Name the blood parasite species.
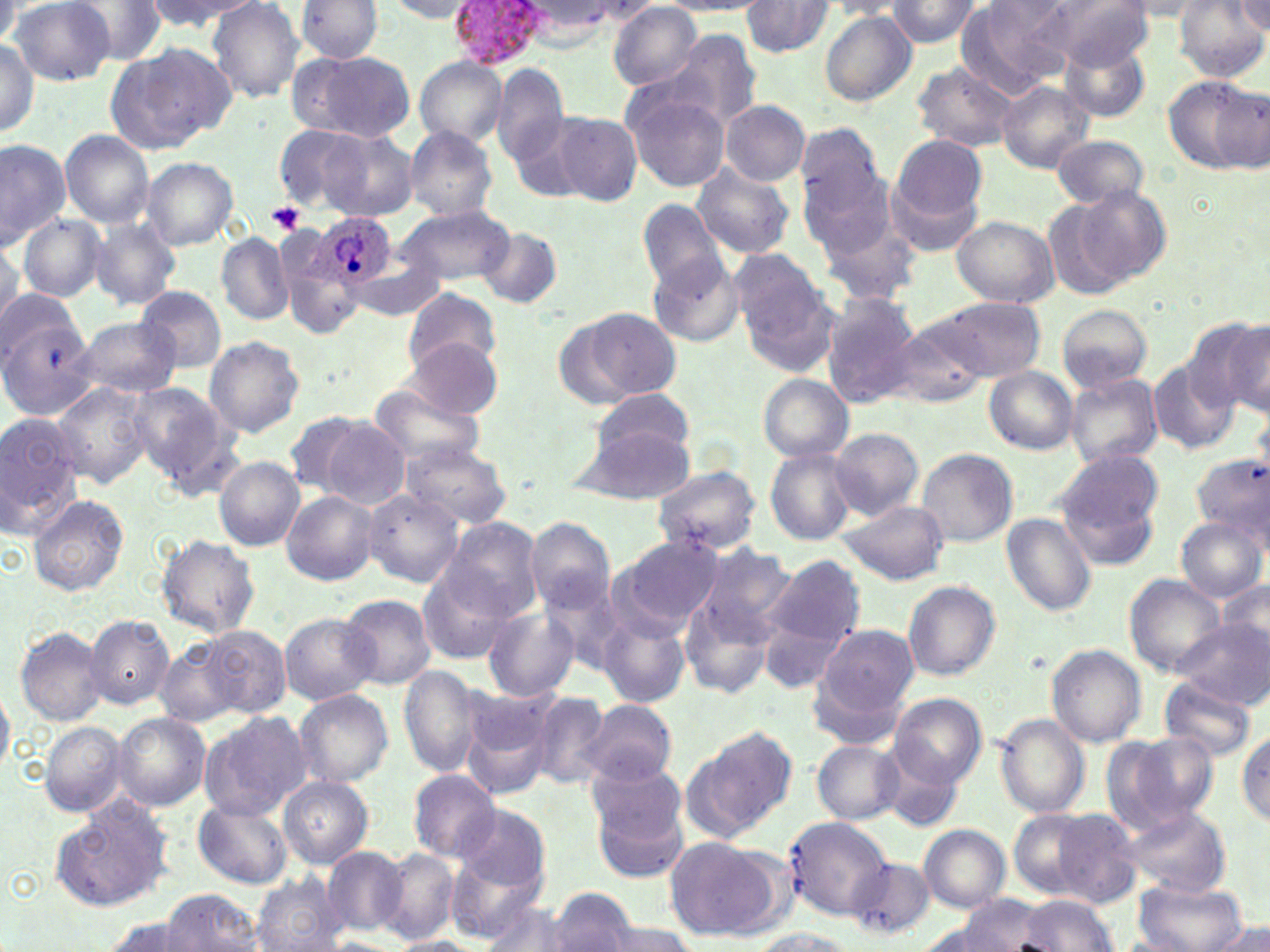

Plasmodium ovale.

Approximate bounding boxes as named x1/y1/x2/y2 corners in pixels. Platelet locations: (x1=267, y1=202, x2=306, y2=234). Plasmodium ovale-infected red blood cell locations: (x1=447, y1=0, x2=550, y2=68), (x1=318, y1=215, x2=396, y2=289). Uninfected red blood cell locations: (x1=9, y1=0, x2=122, y2=83), (x1=67, y1=0, x2=170, y2=62), (x1=139, y1=0, x2=259, y2=33), (x1=294, y1=0, x2=384, y2=63), (x1=884, y1=0, x2=983, y2=47), (x1=954, y1=0, x2=1068, y2=95), (x1=1046, y1=0, x2=1151, y2=71), (x1=1233, y1=0, x2=1269, y2=36), (x1=207, y1=1, x2=307, y2=104), (x1=384, y1=1, x2=480, y2=22), (x1=661, y1=1, x2=774, y2=16), (x1=1117, y1=1, x2=1214, y2=19), (x1=1177, y1=1, x2=1266, y2=82), (x1=741, y1=2, x2=834, y2=57), (x1=823, y1=2, x2=907, y2=18), (x1=609, y1=4, x2=703, y2=88), (x1=819, y1=11, x2=915, y2=106), (x1=662, y1=30, x2=762, y2=132), (x1=1, y1=37, x2=41, y2=135), (x1=1058, y1=38, x2=1148, y2=123), (x1=105, y1=42, x2=235, y2=153), (x1=292, y1=51, x2=416, y2=142), (x1=415, y1=57, x2=507, y2=148), (x1=910, y1=62, x2=1020, y2=152), (x1=493, y1=66, x2=569, y2=167), (x1=1161, y1=74, x2=1266, y2=175), (x1=997, y1=80, x2=1093, y2=174), (x1=619, y1=84, x2=731, y2=193), (x1=721, y1=100, x2=810, y2=185), (x1=546, y1=111, x2=642, y2=206), (x1=794, y1=123, x2=887, y2=217), (x1=275, y1=125, x2=366, y2=210), (x1=404, y1=125, x2=498, y2=220), (x1=316, y1=126, x2=421, y2=222), (x1=60, y1=130, x2=155, y2=228), (x1=891, y1=134, x2=987, y2=228), (x1=1051, y1=135, x2=1148, y2=208), (x1=0, y1=137, x2=71, y2=251), (x1=798, y1=156, x2=899, y2=260), (x1=141, y1=157, x2=239, y2=249), (x1=691, y1=163, x2=795, y2=259), (x1=886, y1=175, x2=983, y2=257), (x1=1072, y1=185, x2=1172, y2=286), (x1=810, y1=195, x2=921, y2=308), (x1=635, y1=198, x2=728, y2=293), (x1=1044, y1=199, x2=1130, y2=302), (x1=397, y1=204, x2=513, y2=287), (x1=17, y1=213, x2=108, y2=304), (x1=951, y1=215, x2=1059, y2=307), (x1=87, y1=219, x2=182, y2=310), (x1=275, y1=224, x2=364, y2=334), (x1=477, y1=227, x2=564, y2=309), (x1=217, y1=233, x2=295, y2=324), (x1=0, y1=235, x2=22, y2=323), (x1=730, y1=249, x2=831, y2=354), (x1=352, y1=250, x2=446, y2=322), (x1=648, y1=255, x2=744, y2=346), (x1=136, y1=286, x2=226, y2=372), (x1=0, y1=287, x2=80, y2=367), (x1=403, y1=287, x2=503, y2=374), (x1=818, y1=293, x2=922, y2=405), (x1=932, y1=296, x2=1045, y2=381), (x1=1055, y1=304, x2=1153, y2=395), (x1=559, y1=308, x2=681, y2=407), (x1=0, y1=315, x2=100, y2=421), (x1=71, y1=315, x2=183, y2=398), (x1=886, y1=316, x2=991, y2=409), (x1=1189, y1=317, x2=1270, y2=416), (x1=203, y1=336, x2=307, y2=438), (x1=400, y1=338, x2=503, y2=420), (x1=1148, y1=359, x2=1240, y2=454), (x1=984, y1=367, x2=1078, y2=455), (x1=1065, y1=373, x2=1163, y2=468), (x1=758, y1=374, x2=853, y2=461), (x1=368, y1=382, x2=485, y2=468), (x1=52, y1=383, x2=151, y2=488), (x1=129, y1=383, x2=229, y2=483), (x1=586, y1=388, x2=698, y2=467), (x1=0, y1=410, x2=88, y2=535), (x1=285, y1=412, x2=367, y2=496), (x1=316, y1=415, x2=411, y2=509), (x1=573, y1=417, x2=696, y2=505), (x1=829, y1=428, x2=924, y2=522), (x1=398, y1=439, x2=510, y2=530), (x1=763, y1=446, x2=858, y2=545), (x1=916, y1=449, x2=1017, y2=549), (x1=1190, y1=452, x2=1270, y2=541), (x1=1054, y1=453, x2=1164, y2=568), (x1=214, y1=456, x2=305, y2=550), (x1=651, y1=466, x2=761, y2=556), (x1=359, y1=489, x2=464, y2=587), (x1=281, y1=492, x2=378, y2=586), (x1=26, y1=494, x2=128, y2=597), (x1=834, y1=499, x2=950, y2=586), (x1=1000, y1=513, x2=1097, y2=616), (x1=1176, y1=515, x2=1266, y2=603), (x1=441, y1=517, x2=543, y2=622), (x1=525, y1=518, x2=615, y2=615), (x1=154, y1=534, x2=260, y2=637), (x1=607, y1=536, x2=724, y2=640), (x1=694, y1=542, x2=797, y2=648), (x1=761, y1=555, x2=863, y2=668), (x1=415, y1=566, x2=517, y2=664), (x1=1123, y1=574, x2=1227, y2=677), (x1=1216, y1=578, x2=1269, y2=661), (x1=901, y1=580, x2=1001, y2=681), (x1=679, y1=590, x2=779, y2=699), (x1=339, y1=593, x2=436, y2=690), (x1=483, y1=605, x2=580, y2=702), (x1=600, y1=612, x2=688, y2=708), (x1=279, y1=613, x2=380, y2=705), (x1=84, y1=615, x2=175, y2=709), (x1=1173, y1=622, x2=1268, y2=708), (x1=814, y1=624, x2=920, y2=724), (x1=14, y1=626, x2=108, y2=725), (x1=204, y1=626, x2=290, y2=717), (x1=157, y1=641, x2=243, y2=727), (x1=1046, y1=645, x2=1147, y2=747), (x1=400, y1=665, x2=482, y2=777), (x1=1159, y1=676, x2=1260, y2=763), (x1=0, y1=685, x2=14, y2=779), (x1=293, y1=689, x2=394, y2=788), (x1=528, y1=690, x2=613, y2=789), (x1=890, y1=692, x2=987, y2=787), (x1=460, y1=693, x2=553, y2=800), (x1=580, y1=698, x2=677, y2=786), (x1=199, y1=711, x2=312, y2=819), (x1=114, y1=713, x2=210, y2=811), (x1=995, y1=714, x2=1090, y2=819), (x1=40, y1=722, x2=127, y2=817), (x1=690, y1=725, x2=798, y2=834), (x1=1236, y1=729, x2=1269, y2=826), (x1=1103, y1=731, x2=1217, y2=834), (x1=812, y1=739, x2=904, y2=826), (x1=881, y1=751, x2=968, y2=832), (x1=587, y1=762, x2=691, y2=873), (x1=408, y1=769, x2=502, y2=862), (x1=278, y1=777, x2=373, y2=867), (x1=47, y1=797, x2=177, y2=913), (x1=194, y1=801, x2=292, y2=888), (x1=1113, y1=802, x2=1230, y2=897), (x1=455, y1=805, x2=551, y2=894), (x1=1007, y1=806, x2=1124, y2=902), (x1=782, y1=815, x2=892, y2=920), (x1=917, y1=823, x2=1010, y2=912), (x1=664, y1=837, x2=774, y2=938), (x1=323, y1=847, x2=408, y2=937), (x1=378, y1=849, x2=460, y2=945), (x1=449, y1=853, x2=546, y2=943), (x1=845, y1=856, x2=934, y2=940), (x1=250, y1=874, x2=348, y2=952), (x1=1132, y1=876, x2=1251, y2=952), (x1=549, y1=886, x2=638, y2=952), (x1=162, y1=889, x2=263, y2=951), (x1=1015, y1=893, x2=1120, y2=950), (x1=957, y1=895, x2=1053, y2=949), (x1=477, y1=901, x2=578, y2=951), (x1=916, y1=910, x2=1028, y2=952), (x1=96, y1=916, x2=199, y2=952), (x1=599, y1=919, x2=698, y2=952), (x1=1205, y1=921, x2=1270, y2=952), (x1=750, y1=929, x2=862, y2=952), (x1=389, y1=937, x2=476, y2=952). Thin blood smear. Image is 1270×952 pixels. Captured at 1000x magnification. One field of a larger specimen. Optical microscopy. May-Grünwald-Giemsa stain.